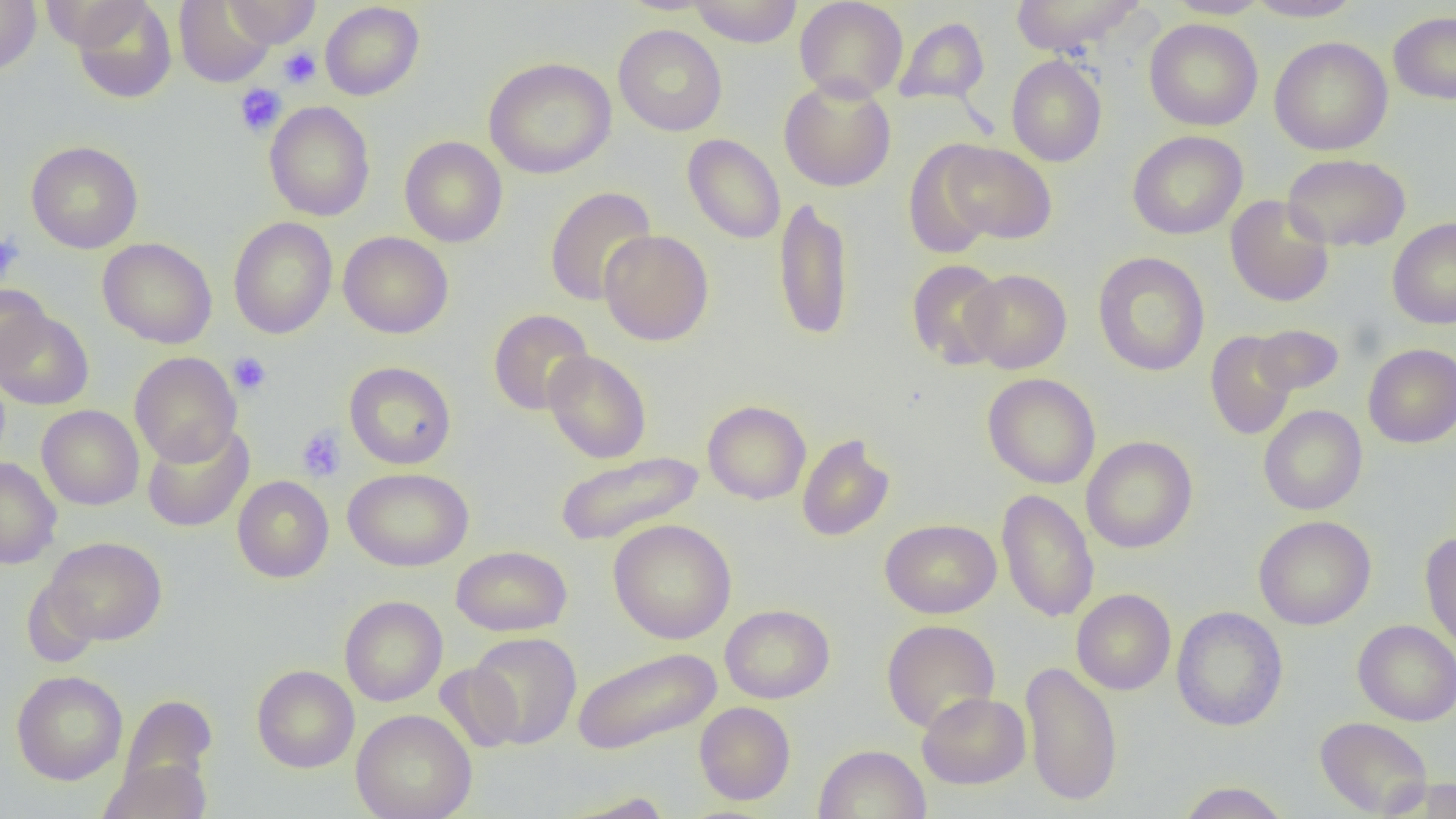
Summary:
  - Coordinate format: approximate bounding boxes as [x1, y1, x2, y2] in pixels
  - Uninfected red blood cell locations: [0, 0, 41, 75], [41, 0, 150, 51], [71, 0, 177, 104], [174, 0, 275, 87], [224, 0, 321, 47], [689, 0, 802, 47], [794, 0, 908, 102], [1009, 0, 1145, 56], [1164, 0, 1271, 18], [1243, 0, 1365, 22], [320, 2, 425, 100], [1388, 11, 1456, 105], [894, 17, 989, 106], [1144, 18, 1263, 131], [613, 25, 727, 136], [1269, 36, 1392, 156], [1006, 55, 1107, 167], [484, 57, 616, 179], [779, 77, 896, 192], [264, 101, 375, 221], [1127, 130, 1248, 240], [682, 134, 786, 244], [400, 136, 508, 247], [26, 140, 143, 254], [903, 140, 1000, 260], [937, 141, 1057, 245], [1282, 153, 1411, 252], [545, 186, 657, 306], [1225, 195, 1334, 307], [773, 196, 854, 341], [228, 216, 338, 339], [1387, 217, 1456, 329], [599, 229, 713, 346], [338, 231, 453, 338], [98, 238, 217, 348], [1093, 252, 1210, 377], [906, 259, 1007, 370], [962, 269, 1072, 374], [0, 283, 51, 377], [0, 309, 94, 410], [489, 309, 594, 415], [1250, 324, 1344, 396], [1205, 331, 1298, 440], [1363, 343, 1456, 448], [543, 350, 652, 463], [129, 352, 242, 466], [344, 361, 456, 469], [982, 373, 1100, 489], [702, 400, 811, 505], [37, 405, 144, 510], [1259, 405, 1367, 515], [142, 423, 254, 532], [797, 433, 895, 541], [1082, 436, 1197, 553], [555, 451, 705, 546], [0, 457, 62, 569], [343, 467, 473, 572], [232, 476, 334, 582], [996, 488, 1099, 623], [1253, 515, 1376, 630], [880, 518, 1001, 618], [608, 519, 737, 644], [1419, 531, 1456, 655], [44, 537, 167, 645], [451, 545, 572, 636], [22, 579, 102, 668], [1072, 588, 1176, 695], [339, 595, 447, 706], [720, 604, 835, 703], [1171, 606, 1288, 731], [881, 619, 1000, 733], [1352, 619, 1456, 726], [467, 631, 581, 749], [571, 648, 722, 755], [1021, 660, 1122, 807], [434, 662, 524, 752], [252, 665, 359, 773], [12, 670, 128, 785], [917, 691, 1031, 789], [119, 694, 217, 796], [694, 702, 796, 805], [351, 709, 477, 819], [1315, 716, 1433, 817], [813, 744, 931, 819], [99, 758, 211, 819], [1383, 777, 1456, 818], [1177, 781, 1292, 818], [563, 791, 674, 818]
  - Platelet locations: [279, 48, 321, 89], [234, 84, 286, 137], [0, 233, 25, 282], [228, 351, 272, 396], [296, 425, 346, 482]
  - Slide-level diagnosis: negative for blood parasites
  - Image size: 1456×819 pixels
  - Field of view: one of a larger specimen
  - Preparation: thin blood smear
  - Magnification: 1000x
  - Modality: optical microscopy